Report the malaria status of this cell.
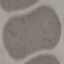

It is uninfected.

Acquired by smartphone through the microscope eyepiece. Automatically extracted cell patch, resized to 64 × 64 pixels. Giemsa-stained preparation. Thin blood film.